Assess this cell for malaria.
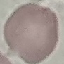
It is uninfected.

Summary:
  - Stain: Giemsa
  - Preparation: thin blood film
  - Capture: smartphone through the microscope eyepiece
  - Image type: automatically extracted cell patch, resized to 64 × 64 pixels